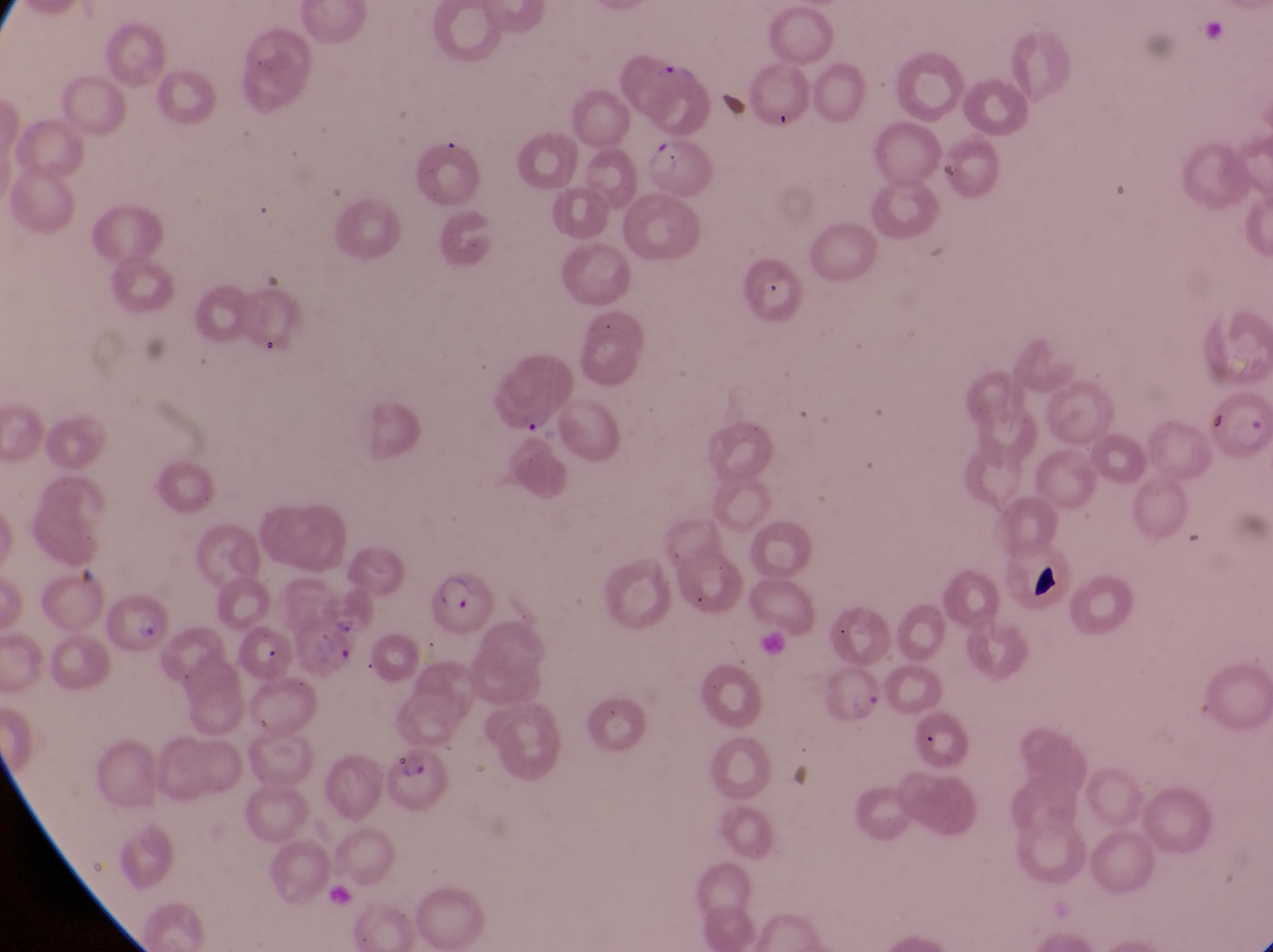

Approximate bounding boxes as (left, top, right, bottom) in pixels.
Summary:
  - Artifact (platelet-like body, stain precipitate, or debris) locations: (1034, 561, 1067, 606)
  - Parasitised red blood cell locations: (717, 88, 764, 136), (651, 137, 720, 205), (488, 362, 575, 436), (1207, 384, 1272, 463), (419, 572, 491, 637), (317, 582, 369, 635), (99, 591, 169, 651), (817, 659, 886, 727), (387, 744, 456, 818)
  - Gametocyte locations: (651, 53, 706, 88)
  - Preparation: thin blood smear
  - Country: Uganda
  - Image size: 1273×952 pixels
  - Field of view: single
  - Capture: smartphone photograph through the eyepiece of an Olympus CX-23 microscope
  - Magnification: 1000x